Describe the morphology of the erythrocytes.
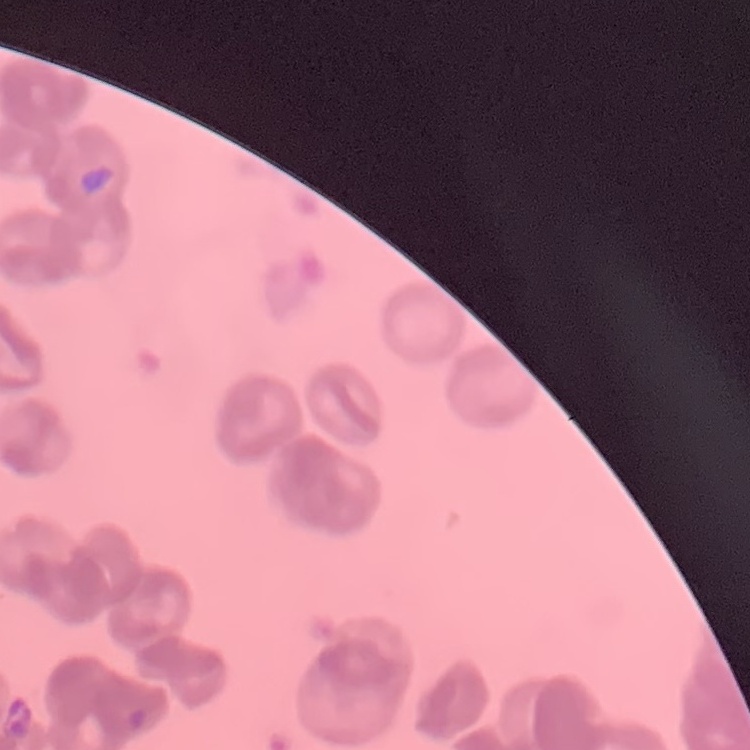
They show rouleaux formation.

Summary:
  - Image type: one tile cut from a larger photomicrograph
  - Stain: Field's or Giemsa
  - Preparation: thin peripheral smear